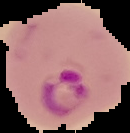

Image is 130×133 pixels. The area outside the segmented cell region is set to black. Result: Plasmodium parasites identified. From a thin blood film.